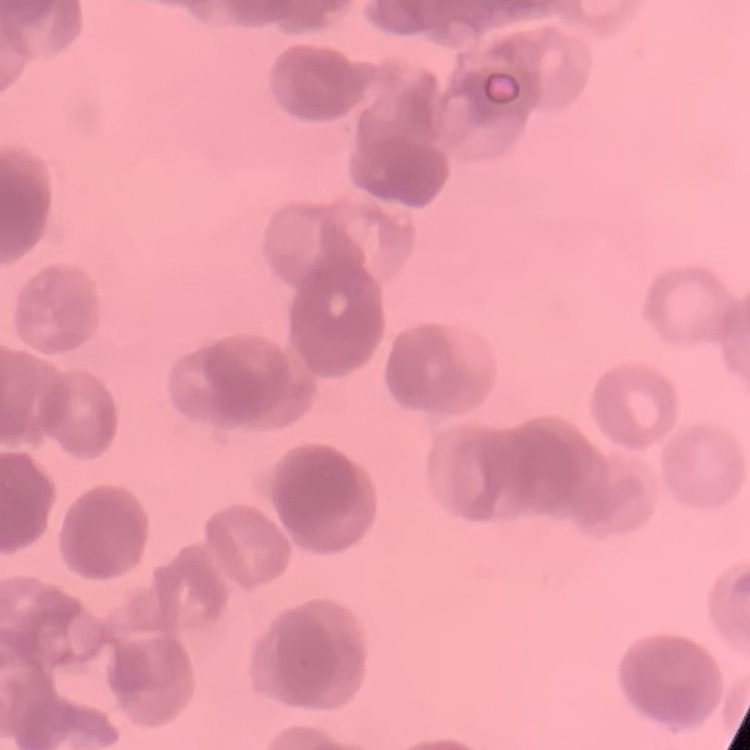

erythrocyte_morphology: rouleaux formation
preparation: thin peripheral smear
image_type: square crop of a larger photomicrograph
stain: Field's or Giemsa